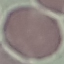 Result: negative for malaria parasites. Acquired by smartphone through the microscope eyepiece. Thin blood smear. Cell patch, automatically extracted from a larger field of view and resized to 64 × 64 pixels. Giemsa stain.